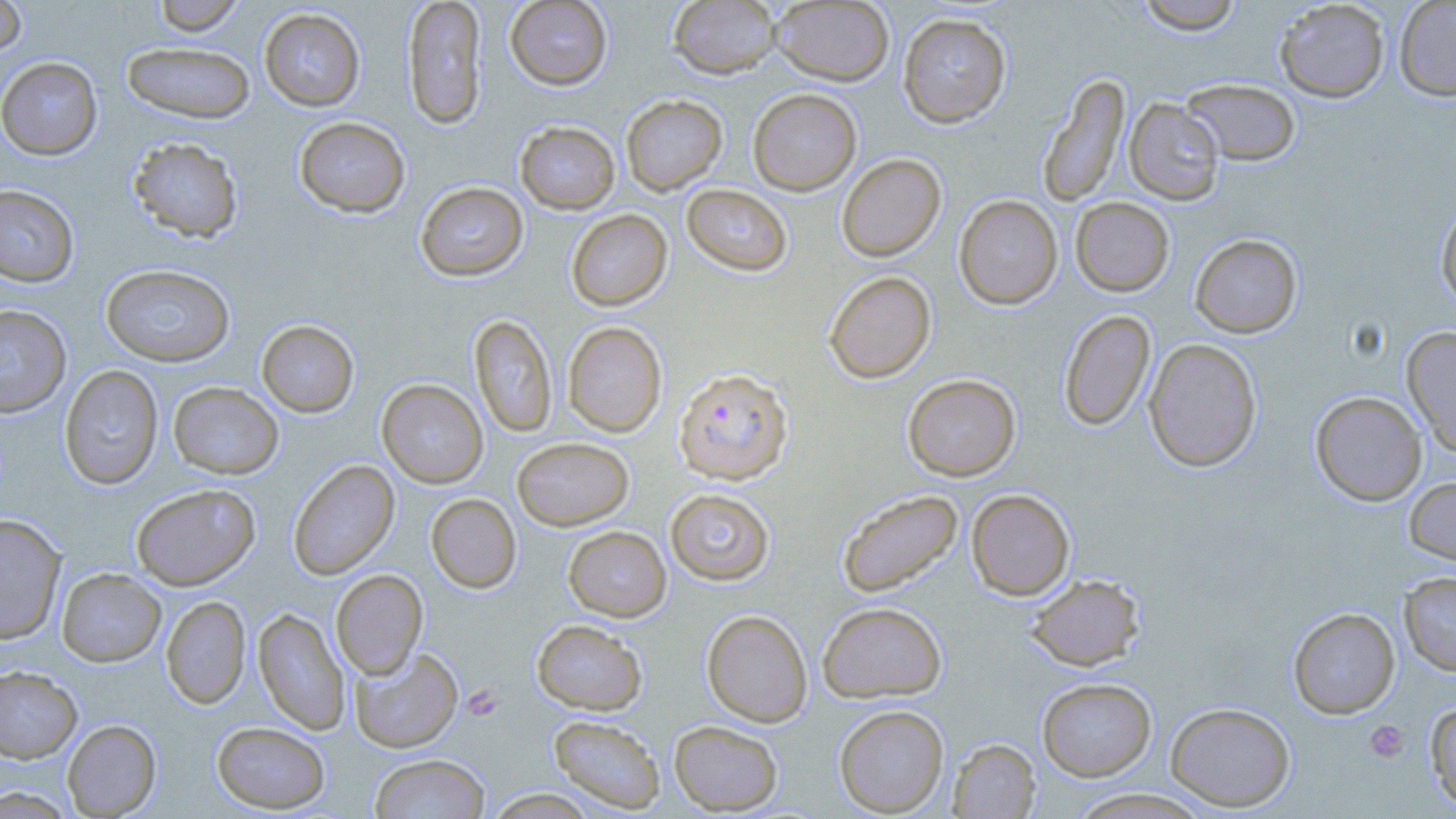
Approximate bounding boxes as [x1, y1, x2, y2] in pixels. Plasmodium falciparum-infected red blood cell locations: [672, 367, 794, 485]. Platelet locations: [462, 685, 502, 721], [1364, 720, 1409, 763]. Uninfected red blood cell locations: [0, 0, 28, 60], [151, 0, 247, 36], [401, 0, 487, 130], [504, 0, 613, 90], [1134, 0, 1245, 34], [1274, 0, 1391, 103], [667, 1, 782, 79], [771, 1, 895, 86], [1393, 1, 1456, 101], [259, 8, 366, 111], [897, 13, 1011, 128], [121, 41, 256, 124], [0, 56, 103, 160], [1037, 74, 1130, 207], [1181, 78, 1301, 166], [747, 88, 862, 195], [621, 95, 727, 195], [1124, 98, 1225, 205], [293, 116, 411, 218], [515, 121, 620, 214], [127, 136, 244, 243], [836, 153, 946, 262], [415, 181, 528, 282], [0, 183, 80, 287], [681, 184, 793, 277], [953, 194, 1063, 310], [1070, 197, 1175, 296], [1435, 201, 1456, 313], [565, 209, 673, 311], [1190, 233, 1303, 338], [100, 264, 235, 367], [823, 270, 937, 384], [0, 305, 71, 417], [1058, 309, 1156, 432], [470, 314, 557, 439], [256, 319, 359, 418], [562, 321, 667, 438], [1401, 326, 1456, 456], [1143, 338, 1262, 472], [59, 365, 163, 490], [902, 373, 1021, 481], [377, 379, 488, 488], [168, 382, 284, 479], [1310, 391, 1427, 506], [512, 437, 634, 530], [288, 460, 400, 580], [1403, 476, 1456, 568], [131, 483, 261, 590], [665, 488, 775, 586], [836, 489, 964, 599], [966, 489, 1075, 600], [425, 494, 522, 594], [0, 513, 66, 645], [563, 526, 672, 621], [56, 568, 166, 667], [331, 569, 428, 679], [1399, 571, 1456, 676], [1025, 574, 1145, 672], [161, 596, 251, 709], [817, 601, 947, 703], [253, 607, 350, 735], [1288, 607, 1400, 719], [701, 609, 813, 727], [532, 619, 647, 715], [350, 646, 463, 753], [0, 665, 82, 763], [1037, 677, 1156, 781], [1423, 699, 1456, 814], [1165, 701, 1296, 811], [834, 705, 949, 817], [547, 714, 666, 814], [62, 719, 162, 817], [669, 720, 784, 815], [212, 721, 330, 813], [948, 738, 1040, 818], [370, 753, 490, 819], [0, 787, 74, 818], [482, 788, 601, 818], [1064, 788, 1213, 818]. Slide-level diagnosis: Plasmodium falciparum. May-Grünwald-Giemsa-stained preparation. One field of a larger specimen. Optical microscopy. Captured at 1000x magnification. Thin blood smear. Image is 1456×819 pixels.